Mark where platelets are.
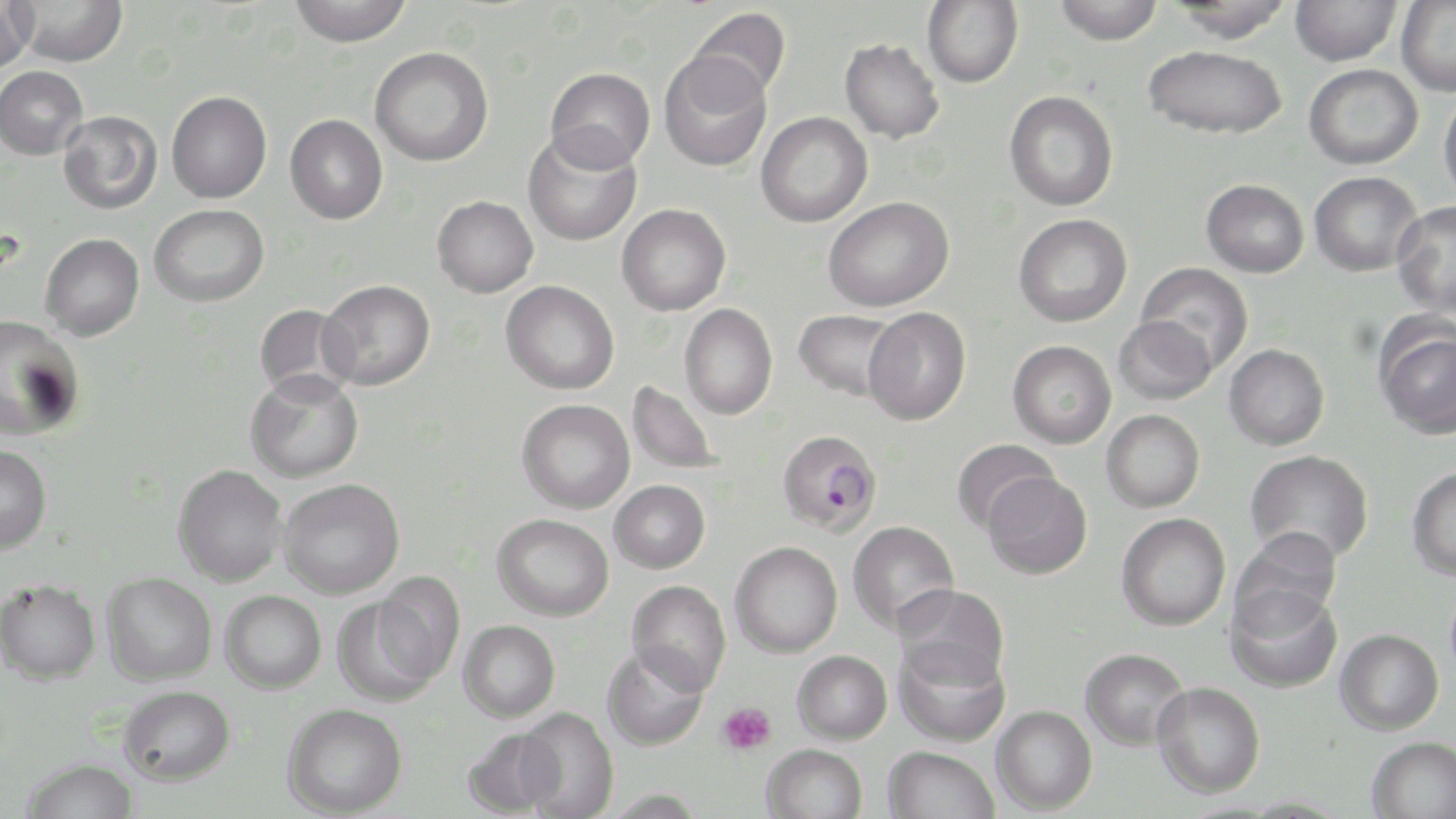
Approximate bounding boxes as [x1, y1, x2, y2] in pixels.
Platelets: [717, 702, 776, 755].

{
  "slide_level_diagnosis": "Plasmodium falciparum",
  "magnification": "1000x",
  "image_size": "1456×819 pixels",
  "field_of_view": "one of a larger specimen",
  "stain": "May-Grünwald-Giemsa",
  "plasmodium_falciparum_infected_red_blood_cell_locations": "approximate bounding boxes as [x1, y1, x2, y2] in pixels: [776, 429, 882, 536]",
  "uninfected_red_blood_cell_locations": "approximate bounding boxes as [x1, y1, x2, y2] in pixels: [9, 0, 128, 66], [289, 0, 412, 47], [922, 0, 1023, 88], [1053, 0, 1164, 45], [1291, 0, 1402, 66], [1396, 0, 1456, 96], [1169, 1, 1294, 42], [0, 2, 36, 73], [687, 7, 790, 101], [840, 38, 944, 143], [1143, 45, 1287, 139], [370, 46, 494, 167], [659, 53, 771, 173], [1304, 64, 1423, 170], [0, 66, 88, 160], [545, 67, 654, 172], [1438, 89, 1456, 207], [166, 90, 272, 203], [1004, 90, 1119, 211], [58, 110, 162, 214], [756, 111, 873, 227], [285, 114, 387, 224], [522, 129, 642, 247], [1309, 171, 1423, 276], [1201, 179, 1309, 277], [432, 195, 538, 297], [823, 197, 954, 312], [1392, 201, 1456, 318], [617, 203, 731, 315], [149, 204, 269, 307], [1013, 214, 1132, 327], [40, 233, 144, 341], [1136, 261, 1255, 373], [318, 279, 435, 390], [501, 280, 619, 394], [253, 303, 357, 402], [679, 304, 778, 420], [863, 307, 971, 425], [793, 309, 903, 401], [1, 315, 85, 441], [1113, 315, 1217, 405], [1374, 318, 1456, 440], [1007, 340, 1116, 448], [1223, 344, 1330, 450], [245, 370, 364, 483], [627, 381, 726, 476], [517, 399, 635, 514], [1101, 409, 1205, 513], [950, 439, 1060, 534], [0, 444, 52, 554], [1244, 450, 1373, 565], [173, 463, 287, 587], [1406, 466, 1456, 581], [983, 472, 1092, 579], [279, 478, 404, 599], [609, 480, 710, 573], [1116, 512, 1231, 630], [492, 513, 614, 621], [847, 521, 959, 635], [1229, 526, 1344, 635], [730, 541, 843, 658], [101, 572, 217, 685], [372, 572, 466, 686], [0, 579, 101, 684], [627, 581, 731, 695], [894, 584, 1010, 691], [1225, 585, 1342, 694], [220, 590, 326, 693], [332, 597, 442, 706], [458, 620, 560, 723], [1334, 628, 1444, 735], [894, 639, 1011, 748], [601, 643, 710, 751], [1080, 647, 1190, 750], [792, 650, 892, 744], [1151, 681, 1265, 798], [118, 685, 235, 786], [282, 703, 408, 817], [992, 705, 1097, 814], [515, 707, 619, 819], [462, 726, 565, 817], [1367, 736, 1456, 819], [761, 744, 867, 819], [883, 746, 999, 819], [21, 758, 139, 819], [603, 789, 706, 818]",
  "preparation": "thin blood film",
  "modality": "optical microscopy"
}